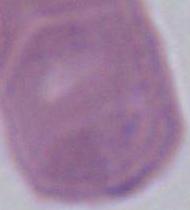
Micrograph. An erythrocyte is seen. Captured at 1000x magnification.